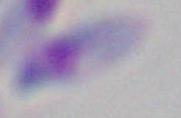
modality = micrograph
magnification = 1000x
identification = Toxoplasma gondii